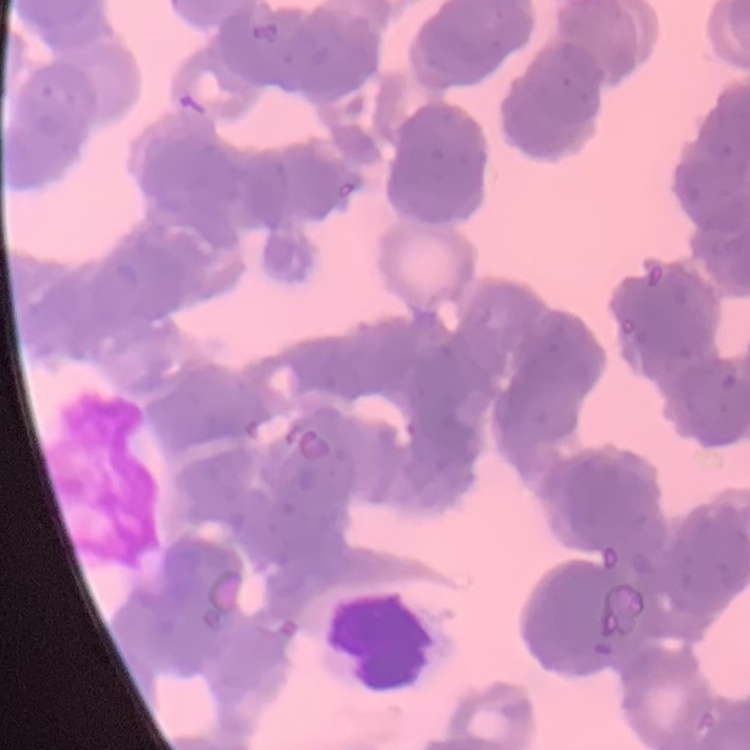

red blood cell morphology = rouleaux formation
stain = Field's or Giemsa
image type = one tile cut from a larger photomicrograph
preparation = thin peripheral smear